Locate every Plasmodium parasite and every leukocyte.
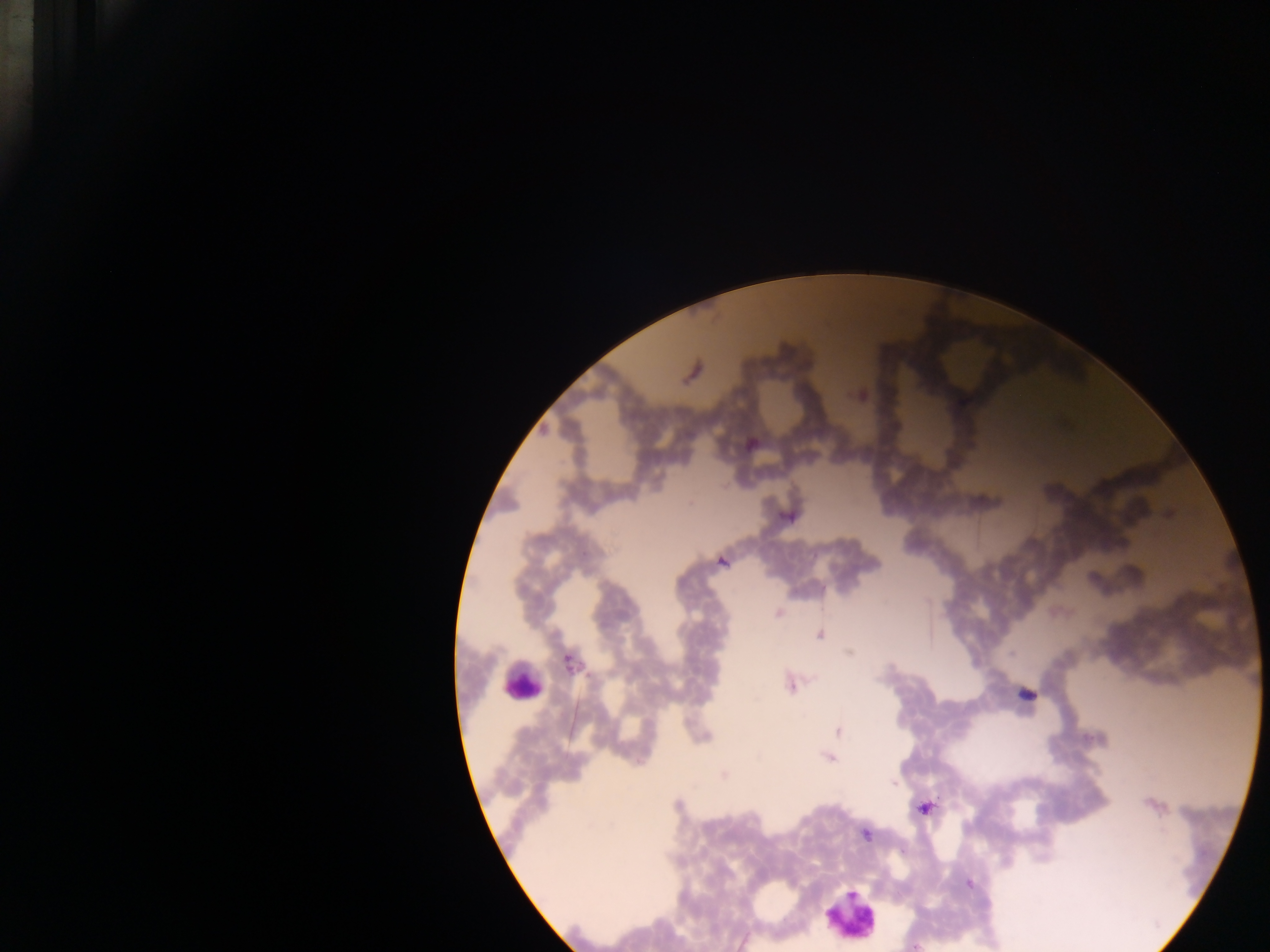

Approximate centers as {x, y} in pixels.
Plasmodium parasites: {693, 371}, {859, 395}, {749, 444}, {1170, 513}, {787, 516}, {722, 561}, {778, 613}, {819, 634}, {850, 652}, {568, 662}, {789, 684}, {1025, 695}, {838, 731}, {829, 756}, {724, 775}, {1154, 804}, {924, 807}, {865, 833}, {969, 883}, {916, 945}.
Leukocytes: {521, 684}, {851, 916}.

Image is 1270×952 pixels. Thick blood film. Sample from Ghana. Single field of view. Mobile-phone photograph taken through the microscope.